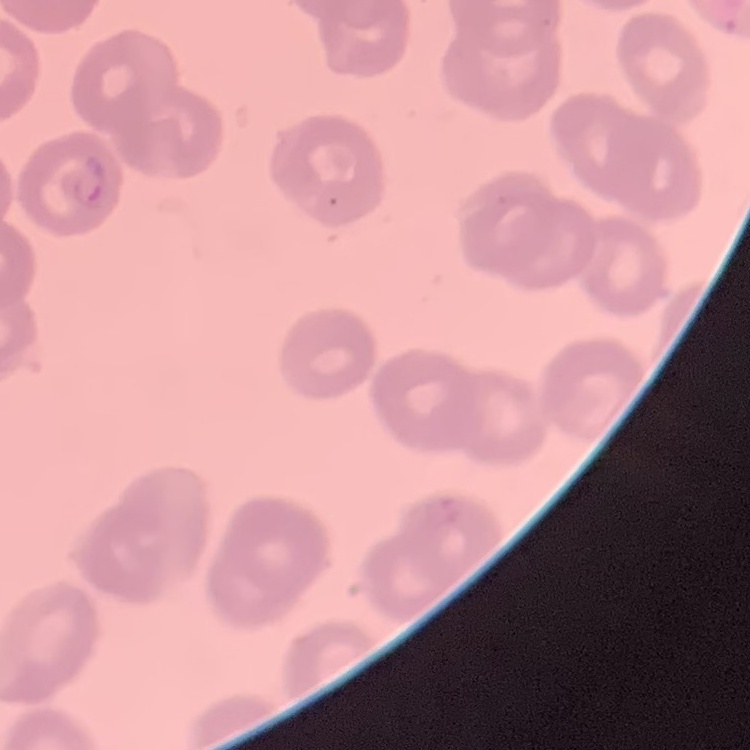
Summary:
  - Erythrocyte morphology: no rouleaux formation
  - Stain: Field's or Giemsa
  - Preparation: thin blood smear
  - Image type: square crop of a larger photomicrograph